Comment on the morphology of the red blood cells.
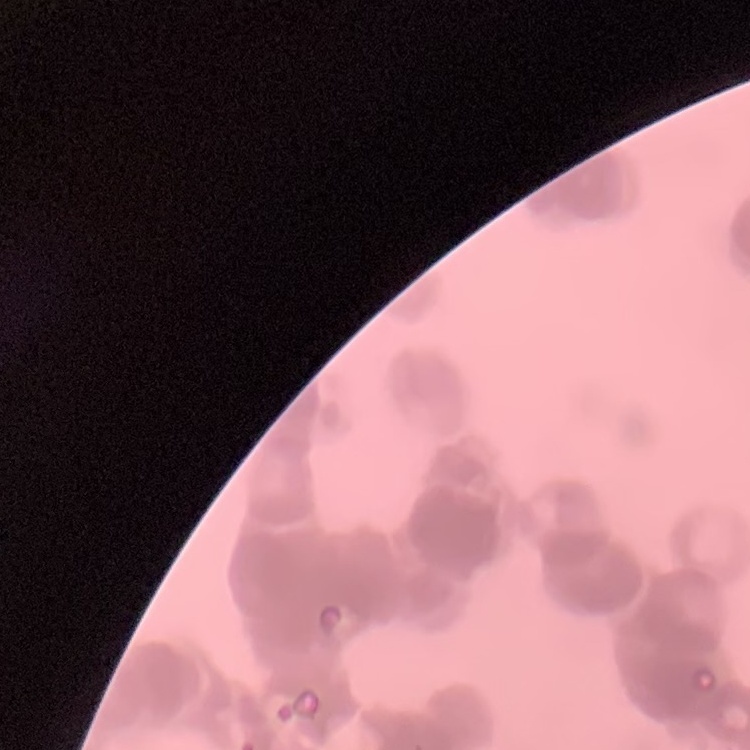

They show rouleaux formation.

Summary:
  - Preparation: thin blood film
  - Image type: one tile cut from a larger photomicrograph
  - Stain: Field's or Giemsa